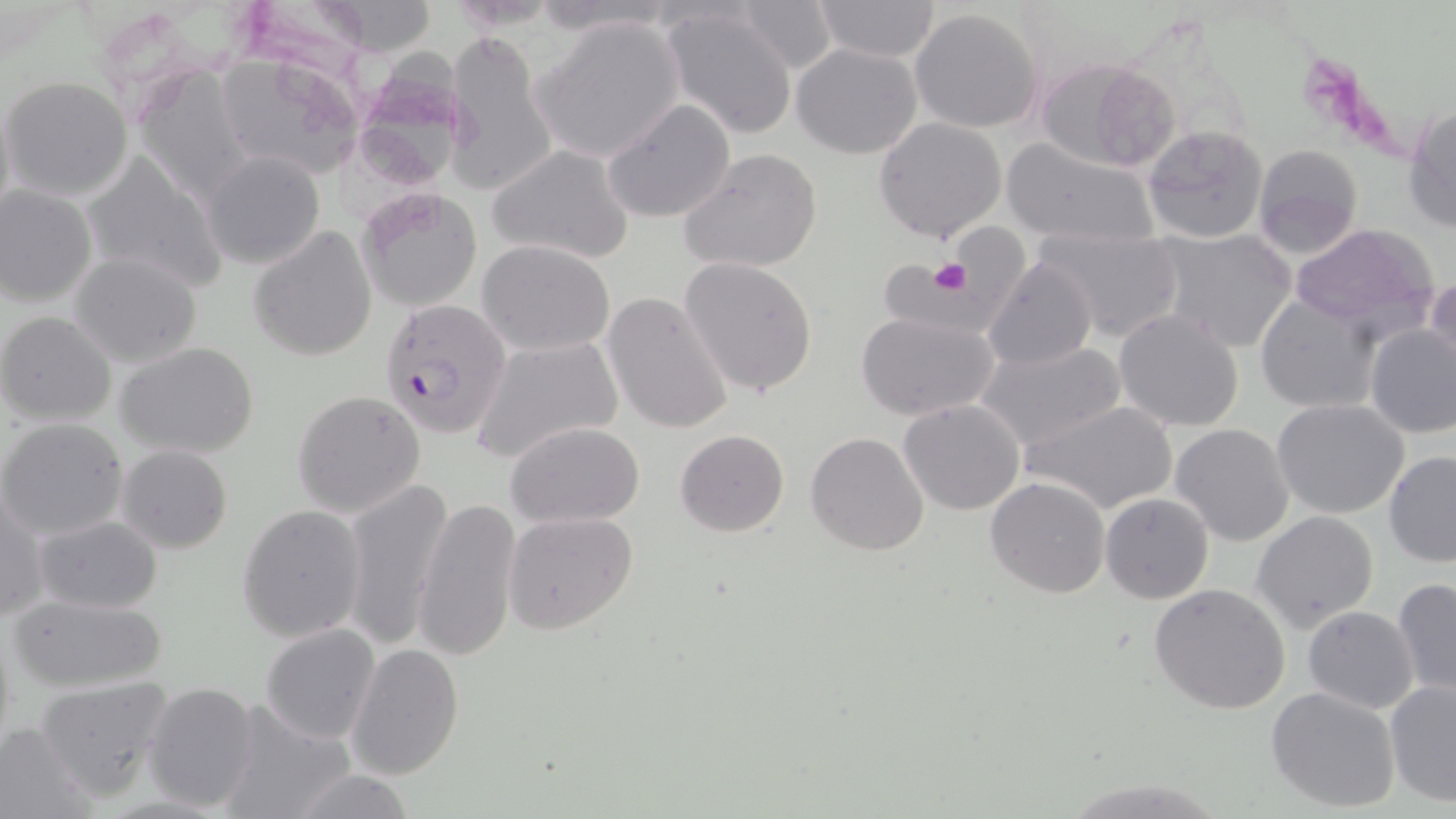
Summary:
  - Coordinate format: approximate bounding boxes as named x1/y1/x2/y2 corners in pixels
  - Uninfected red blood cell locations: (x1=812, y1=0, x2=943, y2=62), (x1=731, y1=1, x2=842, y2=71), (x1=661, y1=4, x2=800, y2=140), (x1=909, y1=7, x2=1044, y2=133), (x1=533, y1=15, x2=685, y2=164), (x1=443, y1=30, x2=554, y2=197), (x1=794, y1=44, x2=922, y2=160), (x1=363, y1=48, x2=457, y2=185), (x1=212, y1=50, x2=364, y2=181), (x1=1038, y1=58, x2=1176, y2=174), (x1=135, y1=70, x2=262, y2=202), (x1=2, y1=75, x2=134, y2=202), (x1=603, y1=98, x2=736, y2=224), (x1=1404, y1=104, x2=1456, y2=232), (x1=873, y1=116, x2=1007, y2=242), (x1=1142, y1=124, x2=1270, y2=245), (x1=1000, y1=136, x2=1160, y2=245), (x1=1250, y1=144, x2=1363, y2=258), (x1=487, y1=147, x2=633, y2=264), (x1=679, y1=148, x2=823, y2=273), (x1=83, y1=151, x2=227, y2=294), (x1=202, y1=151, x2=326, y2=271), (x1=0, y1=184, x2=97, y2=307), (x1=358, y1=189, x2=482, y2=310), (x1=878, y1=221, x2=1039, y2=330), (x1=1290, y1=223, x2=1440, y2=335), (x1=248, y1=224, x2=378, y2=361), (x1=1030, y1=227, x2=1187, y2=344), (x1=1154, y1=228, x2=1300, y2=355), (x1=479, y1=240, x2=616, y2=355), (x1=70, y1=251, x2=201, y2=368), (x1=680, y1=257, x2=819, y2=396), (x1=984, y1=257, x2=1096, y2=370), (x1=1425, y1=275, x2=1455, y2=381), (x1=603, y1=291, x2=733, y2=435), (x1=1255, y1=294, x2=1381, y2=412), (x1=1113, y1=308, x2=1245, y2=432), (x1=0, y1=312, x2=117, y2=427), (x1=857, y1=313, x2=998, y2=421), (x1=1363, y1=323, x2=1456, y2=439), (x1=470, y1=334, x2=623, y2=465), (x1=974, y1=339, x2=1126, y2=454), (x1=116, y1=342, x2=260, y2=458), (x1=291, y1=389, x2=426, y2=519), (x1=899, y1=398, x2=1024, y2=515), (x1=1025, y1=399, x2=1179, y2=515), (x1=1272, y1=399, x2=1410, y2=519), (x1=0, y1=417, x2=129, y2=539), (x1=505, y1=422, x2=644, y2=527), (x1=1170, y1=423, x2=1295, y2=548), (x1=674, y1=428, x2=790, y2=537), (x1=806, y1=432, x2=929, y2=556), (x1=116, y1=444, x2=234, y2=553), (x1=1384, y1=452, x2=1456, y2=565), (x1=338, y1=477, x2=453, y2=653), (x1=986, y1=477, x2=1111, y2=599), (x1=1, y1=492, x2=49, y2=623), (x1=1100, y1=493, x2=1213, y2=604), (x1=412, y1=499, x2=522, y2=663), (x1=236, y1=504, x2=366, y2=642), (x1=503, y1=510, x2=637, y2=634), (x1=1251, y1=510, x2=1380, y2=630), (x1=32, y1=515, x2=162, y2=614), (x1=1392, y1=577, x2=1455, y2=700), (x1=1149, y1=583, x2=1291, y2=714), (x1=8, y1=593, x2=168, y2=694), (x1=1302, y1=606, x2=1418, y2=713), (x1=260, y1=624, x2=381, y2=745), (x1=346, y1=643, x2=465, y2=780), (x1=35, y1=676, x2=173, y2=802), (x1=1384, y1=679, x2=1456, y2=807), (x1=143, y1=681, x2=263, y2=813), (x1=1266, y1=685, x2=1402, y2=812), (x1=212, y1=702, x2=357, y2=818), (x1=0, y1=721, x2=96, y2=817), (x1=285, y1=771, x2=418, y2=817)
  - Platelet locations: (x1=928, y1=257, x2=972, y2=296)
  - Plasmodium falciparum-infected red blood cell locations: (x1=381, y1=298, x2=512, y2=438)
  - Slide-level diagnosis: Plasmodium falciparum
  - Magnification: 1000x
  - Field of view: one of a larger specimen
  - Modality: light microscopy
  - Preparation: thin blood smear
  - Image size: 1456×819 pixels
  - Stain: May-Grünwald-Giemsa